Classify this cell by malaria status.
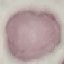

It is uninfected.

Summary:
  - Preparation: thin blood film
  - Image type: cell patch, automatically extracted from a larger field of view and resized to 64 × 64 pixels
  - Capture: smartphone camera at the microscope eyepiece
  - Stain: Giemsa